State which parasite is depicted.
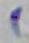

Toxoplasma gondii.

Summary:
  - Magnification: 1000x
  - Modality: micrograph